Report the malaria status of this cell.
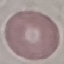

Uninfected.

Summary:
  - Stain: Giemsa
  - Preparation: thin blood film
  - Capture: smartphone through the microscope eyepiece
  - Image type: cell patch, automatically extracted from a larger field of view and resized to 64 × 64 pixels